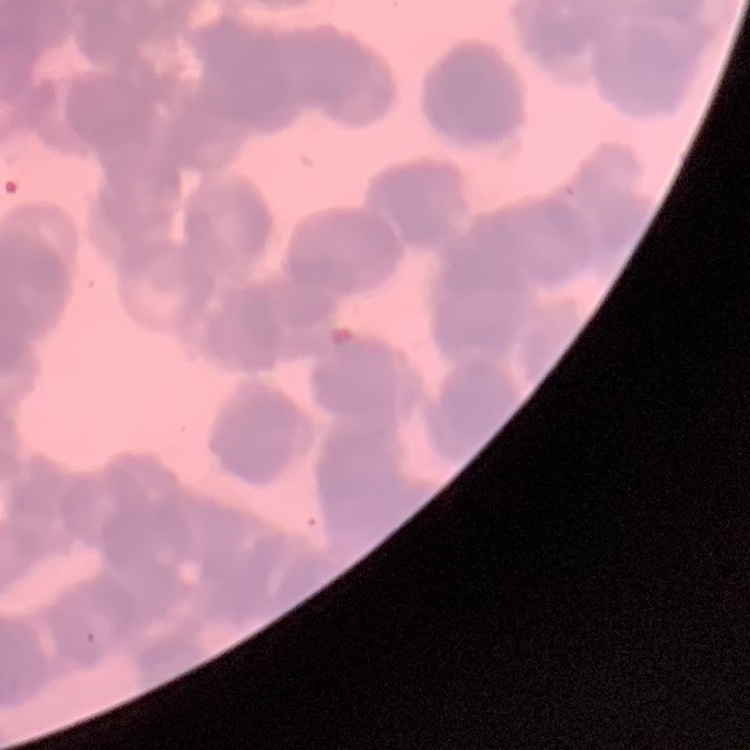
red blood cell morphology = rouleaux formation
stain = Field's or Giemsa
preparation = thin blood smear
image type = square crop of a larger photomicrograph